Give the position of every Plasmodium parasite.
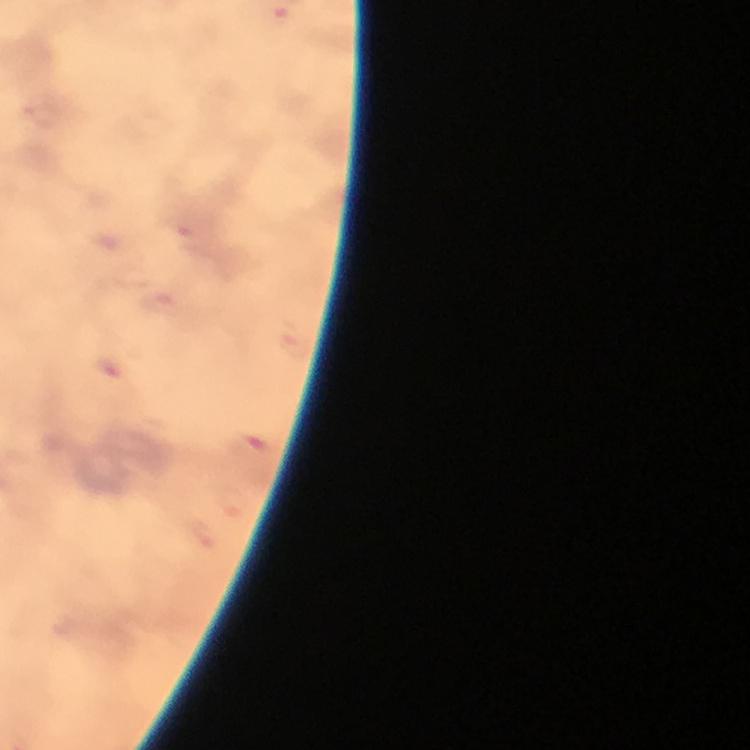
Approximate centers as {x, y} in pixels.
Plasmodium parasites: {113, 368}, {252, 445}.

Immersion oil applied. Smartphone photograph taken through a microscope. Image is 750×750 pixels. Giemsa stain. 100x magnification. Cropped region of a single field of view. From a malaria diagnostic workup. Thick blood film.